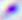

Summary:
  - Magnification: 400x
  - Identification: Toxoplasma gondii
  - Modality: photomicrograph